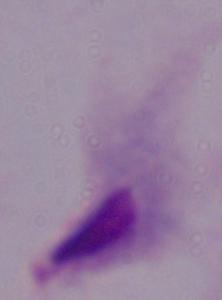 A trichomonad is seen. Photomicrograph. 1000x magnification.